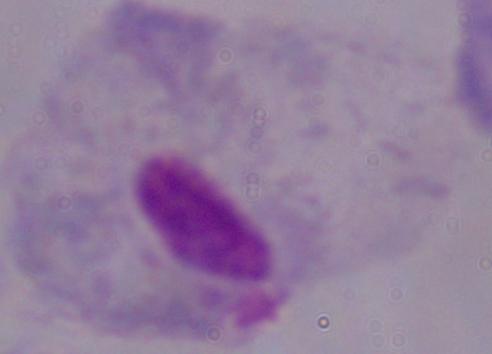
Summary:
  - Magnification: 1000x
  - Identification: trichomonad
  - Modality: photomicrograph